Identify the cell.
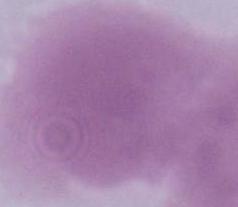

An erythrocyte.

modality = photomicrograph
magnification = 1000x